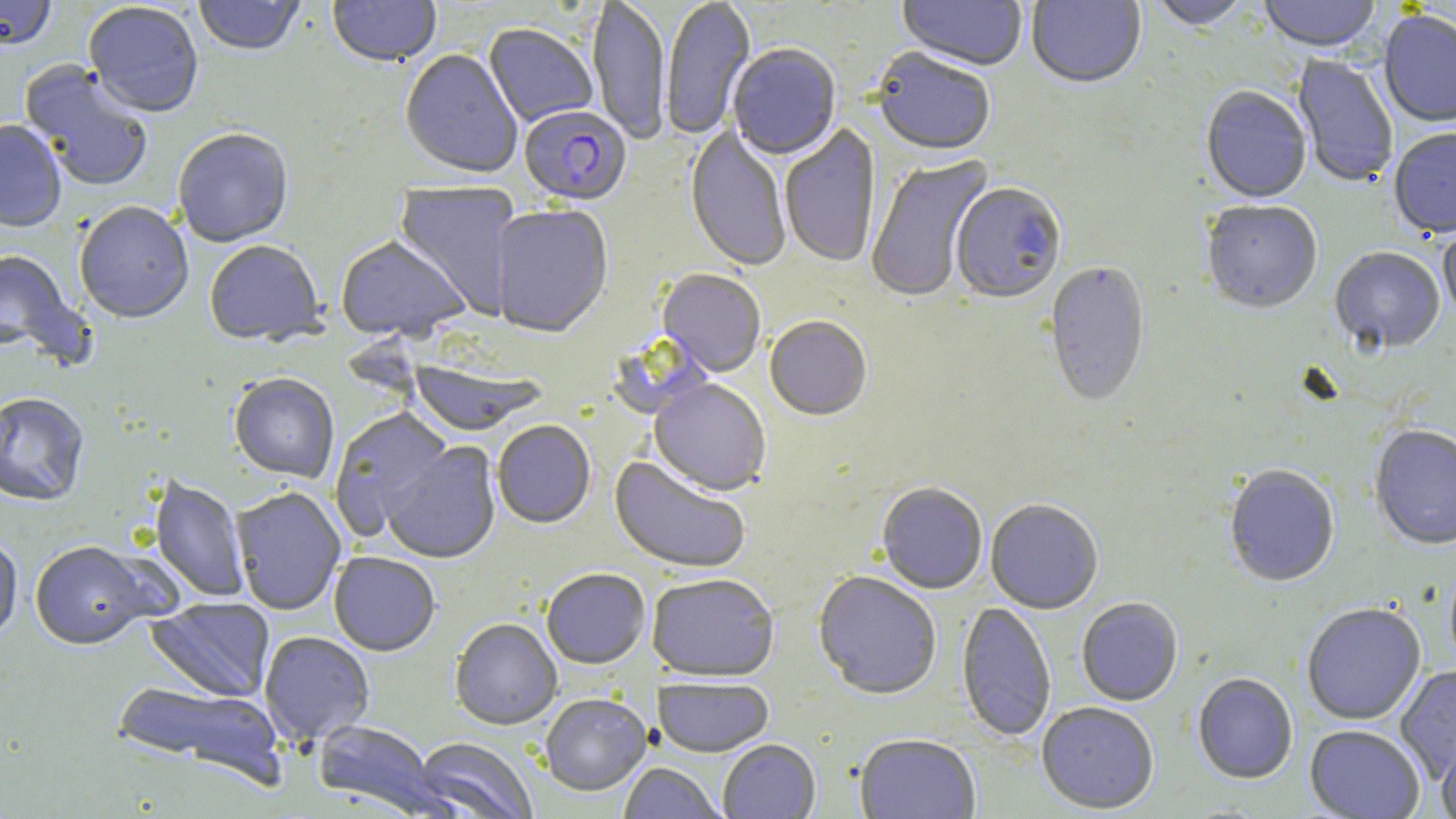

{
  "slide_level_diagnosis": "Plasmodium falciparum",
  "uninfected_red_blood_cell_locations": "approximate bounding boxes as (x1,y1)-(x2,y2) corner pairs in pixels: (0,0)-(57,53), (193,0)-(306,59), (327,0)-(441,69), (587,0)-(671,147), (661,0)-(755,142), (897,0)-(1027,73), (1026,0)-(1146,91), (1257,0)-(1383,55), (1147,1)-(1255,33), (83,3)-(203,121), (1379,11)-(1456,129), (483,25)-(597,128), (727,46)-(841,162), (400,50)-(522,180), (871,50)-(995,159), (1292,55)-(1398,188), (18,60)-(154,194), (1200,87)-(1311,205), (0,122)-(66,234), (780,125)-(880,269), (685,126)-(791,273), (173,130)-(293,249), (1389,130)-(1456,241), (866,154)-(995,305), (393,181)-(521,318), (951,184)-(1067,307), (1201,202)-(1322,317), (75,203)-(193,326), (491,206)-(613,340), (1438,226)-(1456,327), (335,237)-(471,345), (205,242)-(326,349), (0,249)-(87,367), (1330,249)-(1444,355), (1044,262)-(1150,409), (657,270)-(766,379), (764,318)-(872,422), (408,359)-(546,437), (229,375)-(339,485), (649,380)-(771,497), (0,394)-(89,508), (330,408)-(454,540), (493,422)-(595,530), (1369,426)-(1456,552), (382,441)-(501,565), (609,456)-(750,575), (1224,467)-(1339,589), (148,477)-(249,604), (877,484)-(987,595), (231,488)-(346,616), (985,500)-(1103,615), (0,538)-(22,648), (29,543)-(157,653), (329,553)-(440,658), (541,570)-(650,670), (812,572)-(942,702), (647,574)-(779,684), (145,598)-(276,704), (1076,599)-(1183,707), (956,602)-(1056,742), (1302,604)-(1426,726), (450,620)-(562,731), (259,632)-(374,746), (1396,666)-(1455,784), (1192,674)-(1297,785), (654,678)-(774,759), (109,680)-(287,787), (540,695)-(651,797), (1037,703)-(1159,815), (312,721)-(440,815), (1305,726)-(1425,819), (1437,735)-(1456,819), (854,736)-(981,819), (412,738)-(537,819), (718,741)-(820,818), (620,763)-(724,819)",
  "plasmodium_falciparum_infected_red_blood_cell_locations": "approximate bounding boxes as (x1,y1)-(x2,y2) corner pairs in pixels: (520,107)-(632,208)",
  "modality": "light microscopy",
  "image_size": "1456×819 pixels",
  "magnification": "1000x",
  "field_of_view": "one of a larger specimen",
  "preparation": "thin blood film",
  "stain": "May-Grünwald-Giemsa"
}